Classify this cell by malaria status.
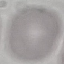
Uninfected.

capture: smartphone camera at the microscope eyepiece
image_type: automatically extracted cell patch, resized to 64 × 64 pixels
stain: Giemsa
preparation: thin blood film